Point out each Plasmodium parasite.
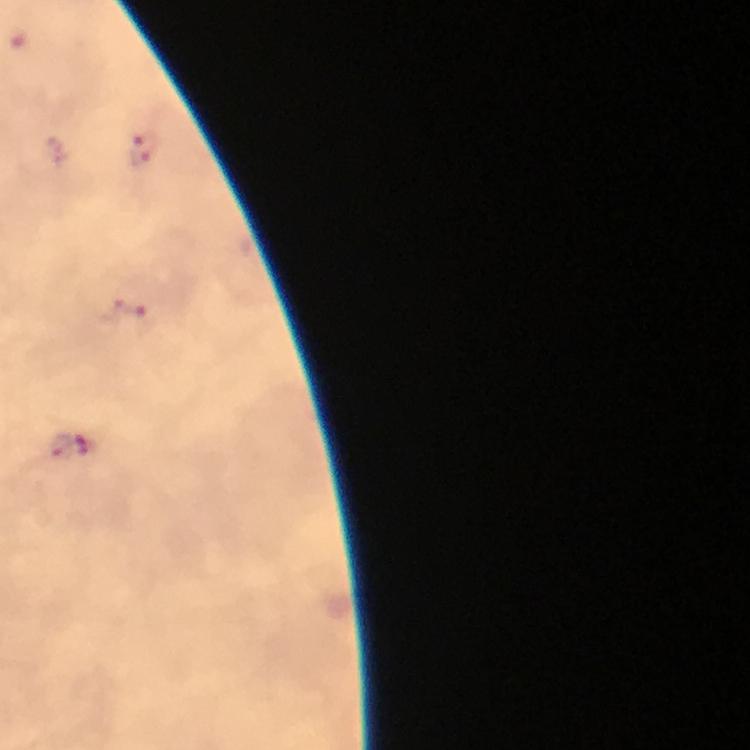

Approximate object centers, in pixels from the top-left corner.
Plasmodium parasites: (x=19, y=42), (x=144, y=150), (x=129, y=307), (x=70, y=446).

From a diagnostic examination for malaria. Image is 750×750 pixels. Thick blood smear. Cropped region of a single field of view. Photographed through the microscope with a smartphone camera. 100x magnification. Immersion oil was used. Giemsa-stained preparation.